Assess this cell for malaria.
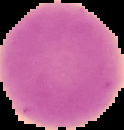

Uninfected.

preparation = thin blood film
image size = 124×130 pixels
image type = segmented cell region on a black background